Report the malaria status of this cell.
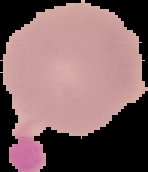
It is uninfected.

image_size: 148×172 pixels
preparation: thin blood film
image_type: cell region segmented out of the field of view; surrounding area masked to black